Identify the cell.
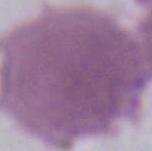
This is an erythrocyte.

Micrograph. 1000x magnification.